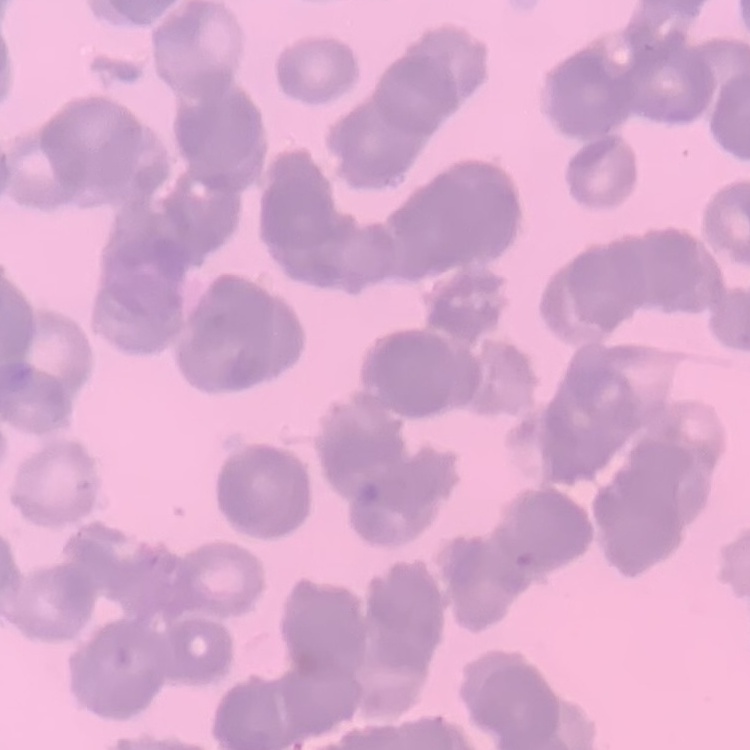
The red blood cells exhibit rouleaux formation. Thin blood film. Field's or Giemsa stain. One tile cut from a larger photomicrograph.